Give the position of every leukocyte visible.
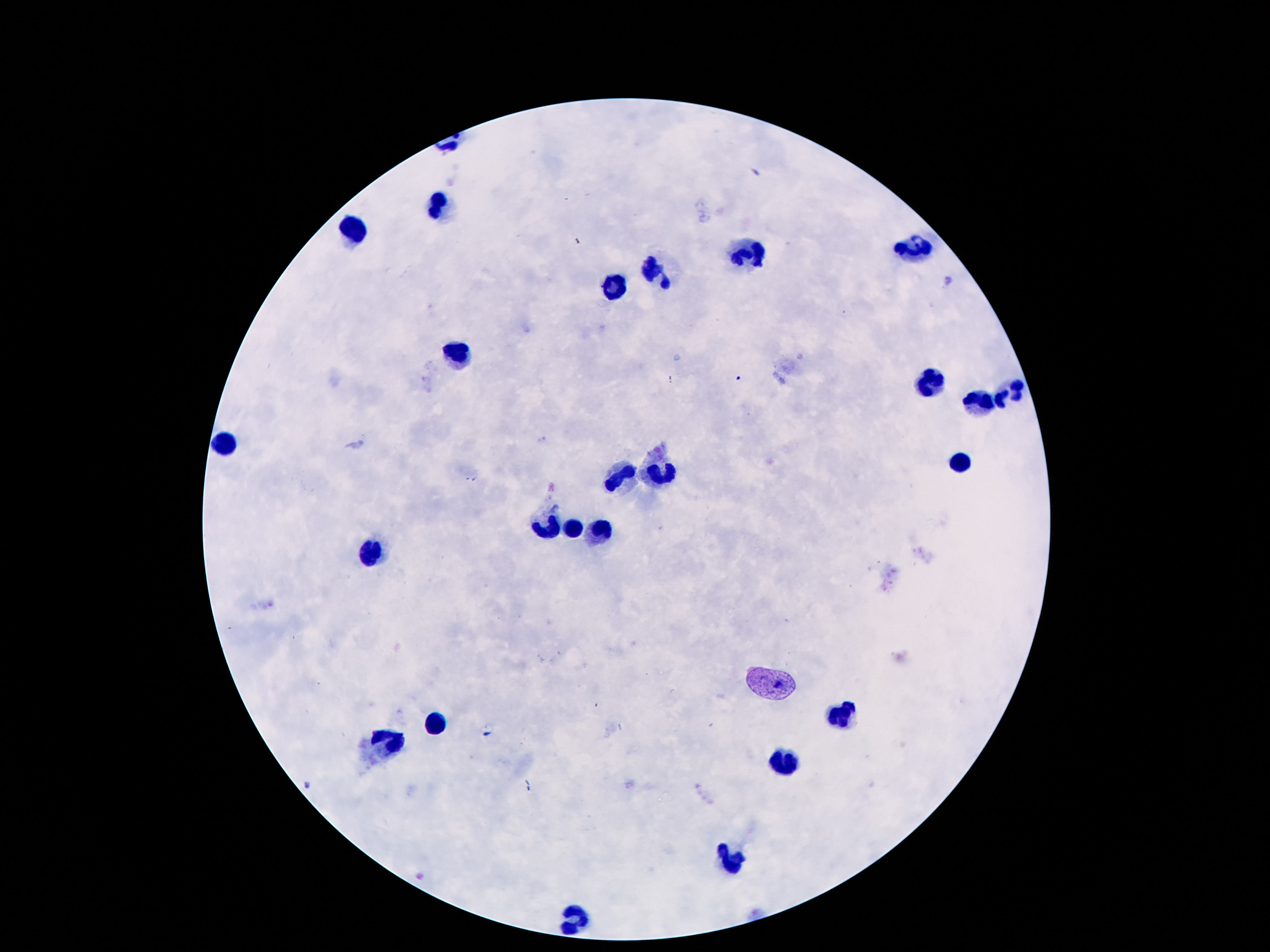
Approximate object centers, in pixels from the top-left corner.
Leukocytes: (x=437, y=205), (x=355, y=232), (x=916, y=247), (x=750, y=253), (x=652, y=271), (x=615, y=289), (x=459, y=353), (x=933, y=377), (x=1017, y=394), (x=980, y=404), (x=224, y=439), (x=961, y=469), (x=621, y=475), (x=662, y=476), (x=554, y=527), (x=574, y=529), (x=595, y=534), (x=371, y=554), (x=843, y=713), (x=435, y=724), (x=384, y=739), (x=785, y=764), (x=732, y=859), (x=574, y=920).

100x magnification. Giemsa-stained preparation. Image is 1270×952 pixels. Patient malaria status: negative. Thick peripheral-blood smear. One field from this slide. Smartphone photograph taken through the microscope eyepiece.